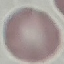
Summary:
  - Malaria status: uninfected
  - Capture: smartphone camera at the microscope eyepiece
  - Preparation: thin smear
  - Stain: Giemsa
  - Image type: cell patch, automatically extracted from a larger field of view and resized to 64 × 64 pixels